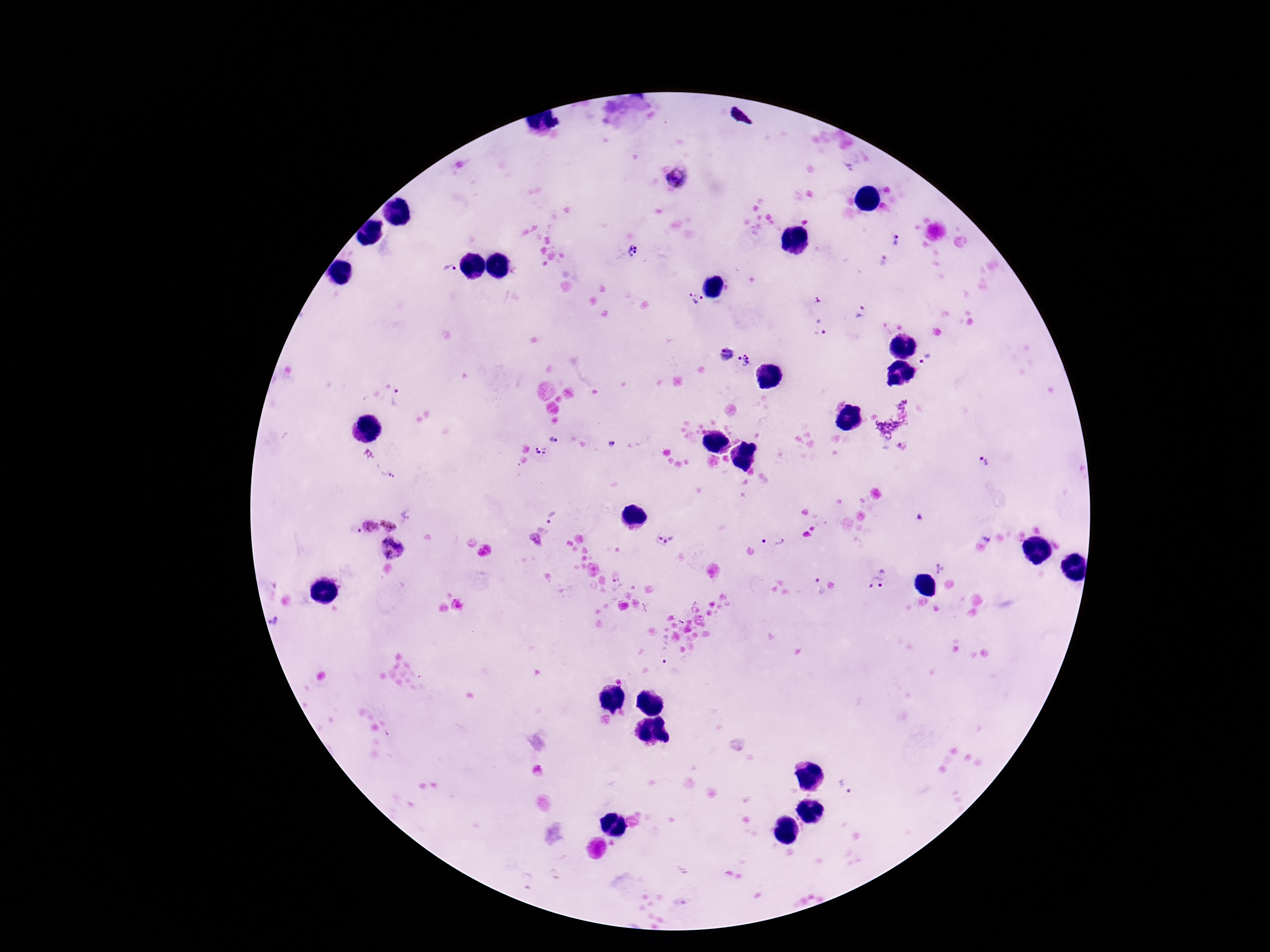

field of view = one from this slide
stain = Giemsa
preparation = thick blood film
magnification = 100x
patient malaria status = positive
Plasmodium parasite locations = approximate centers as (x, y) in pixels: (675, 178), (896, 241), (632, 250), (884, 262), (449, 269), (695, 298), (817, 300), (859, 311), (821, 326), (726, 354), (743, 360), (928, 360), (398, 398), (553, 439), (612, 444), (541, 452), (983, 461), (387, 472), (920, 517), (551, 518), (390, 523), (368, 526), (665, 539), (986, 539), (774, 542), (391, 548), (940, 568), (878, 578), (817, 587), (663, 654), (847, 786)
image size = 1270×952 pixels
capture = smartphone camera through the microscope eyepiece